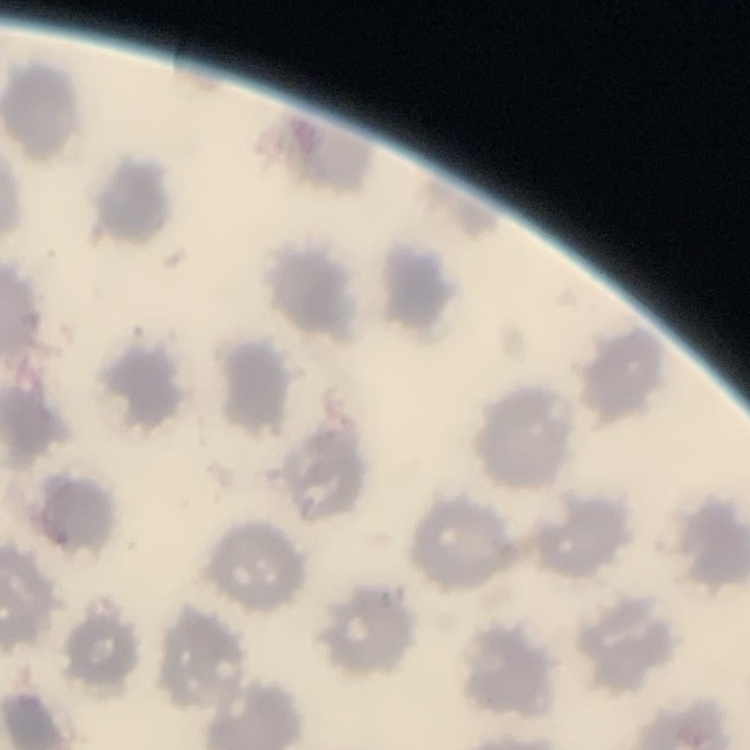 The erythrocytes exhibit no rouleaux formation. One tile cut from a larger photomicrograph. Field's or Giemsa stain. Thin blood smear.